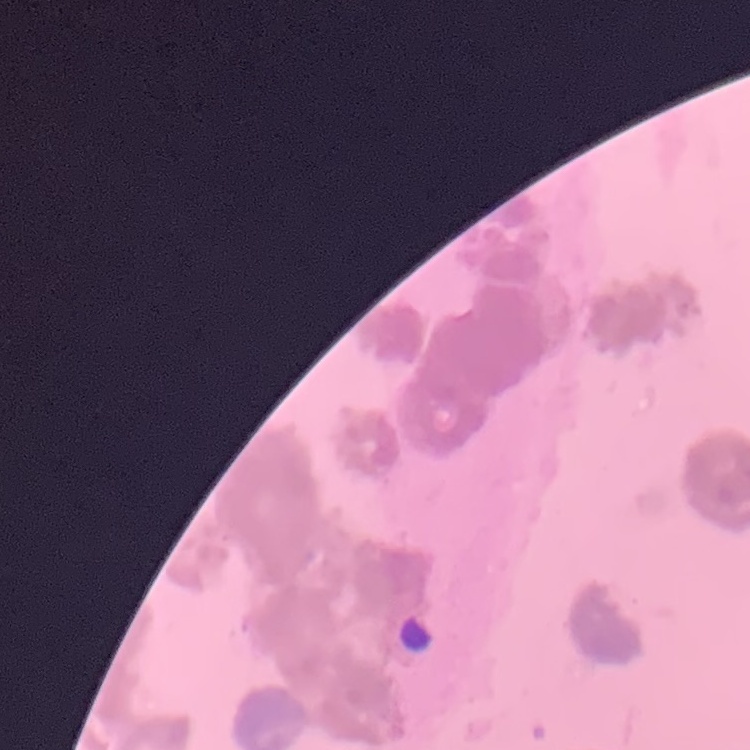

Summary:
  - Erythrocyte morphology: rouleaux formation
  - Stain: Field's or Giemsa
  - Preparation: thin blood smear
  - Image type: one tile cut from a larger photomicrograph